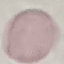

Summary:
  - Malaria status: uninfected
  - Stain: Giemsa
  - Capture: smartphone through the microscope eyepiece
  - Preparation: thin blood film
  - Image type: automatically extracted cell patch, resized to 64 × 64 pixels